Describe the morphology of the red blood cells.
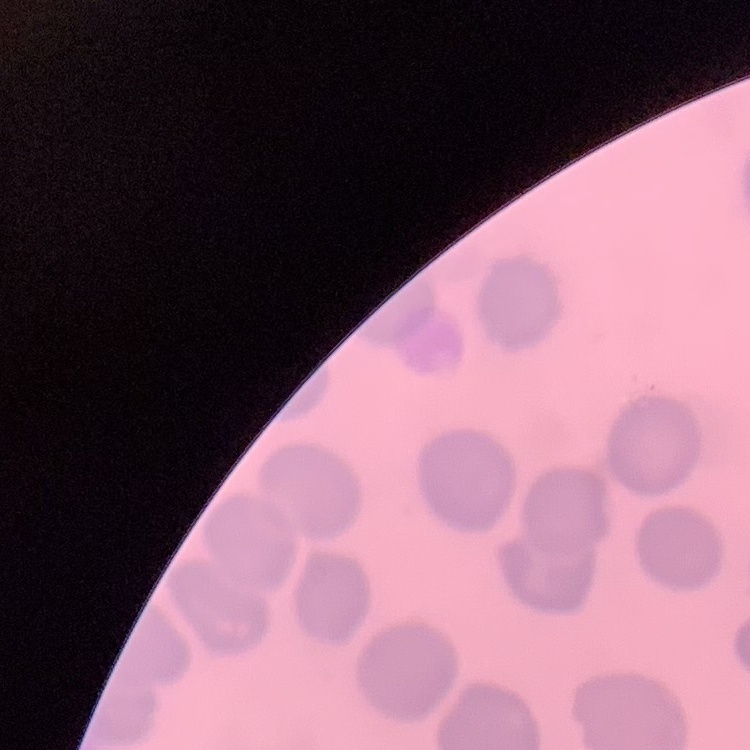

They show no rouleaux formation.

Thin peripheral smear. Square crop of a larger photomicrograph. Field's or Giemsa stain.